Name the blood parasite species.
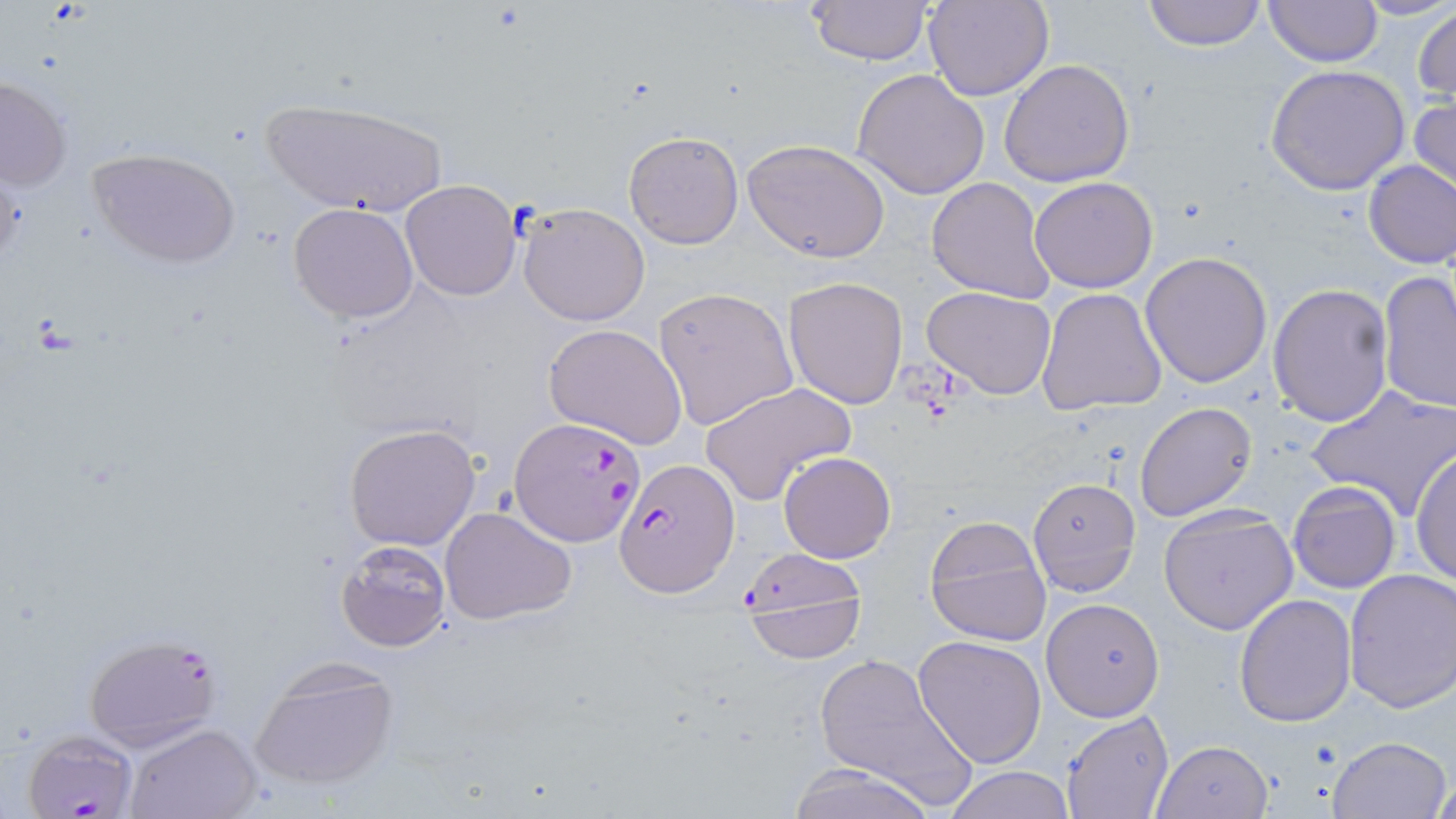
Plasmodium falciparum.

Summary:
  - Coordinate format: approximate bounding boxes as (x1,y1)-(x2,y2) corner pairs in pixels
  - Uninfected red blood cell locations: (806,0)-(933,66), (926,0)-(1054,102), (1139,0)-(1269,49), (1263,0)-(1382,68), (1413,4)-(1456,107), (998,59)-(1136,188), (1265,64)-(1411,194), (852,67)-(990,198), (1,75)-(73,195), (1409,95)-(1456,204), (260,99)-(449,217), (623,130)-(744,248), (742,140)-(890,263), (88,146)-(241,269), (1363,162)-(1456,268), (1029,176)-(1159,293), (927,177)-(1056,304), (399,180)-(522,301), (288,202)-(420,323), (517,202)-(650,326), (1140,251)-(1273,390), (1378,272)-(1456,414), (784,276)-(909,409), (1268,284)-(1395,427), (923,285)-(1057,399), (652,286)-(798,432), (1037,287)-(1168,416), (543,322)-(690,452), (699,381)-(855,505), (1306,385)-(1456,520), (1133,401)-(1258,522), (343,423)-(480,551), (1410,446)-(1456,590), (778,452)-(895,564), (1027,477)-(1141,597), (1288,482)-(1401,595), (439,506)-(579,627), (1157,506)-(1297,636), (923,514)-(1052,647), (335,539)-(452,652), (1342,567)-(1456,712), (1234,593)-(1359,727), (1040,598)-(1166,720), (913,635)-(1047,768), (809,647)-(979,810), (247,657)-(401,791), (1062,712)-(1174,819), (124,723)-(261,819), (1327,736)-(1454,819), (1153,739)-(1273,818), (784,763)-(936,819), (942,766)-(1074,819), (1430,773)-(1456,818)
  - Plasmodium falciparum-infected red blood cell locations: (511,419)-(645,545), (613,458)-(738,598), (738,556)-(865,664), (82,631)-(223,751), (20,730)-(139,819)
  - Image size: 1456×819 pixels
  - Preparation: thin blood film
  - Modality: optical microscopy
  - Magnification: 1000x
  - Stain: May-Grünwald-Giemsa
  - Field of view: one of a larger specimen